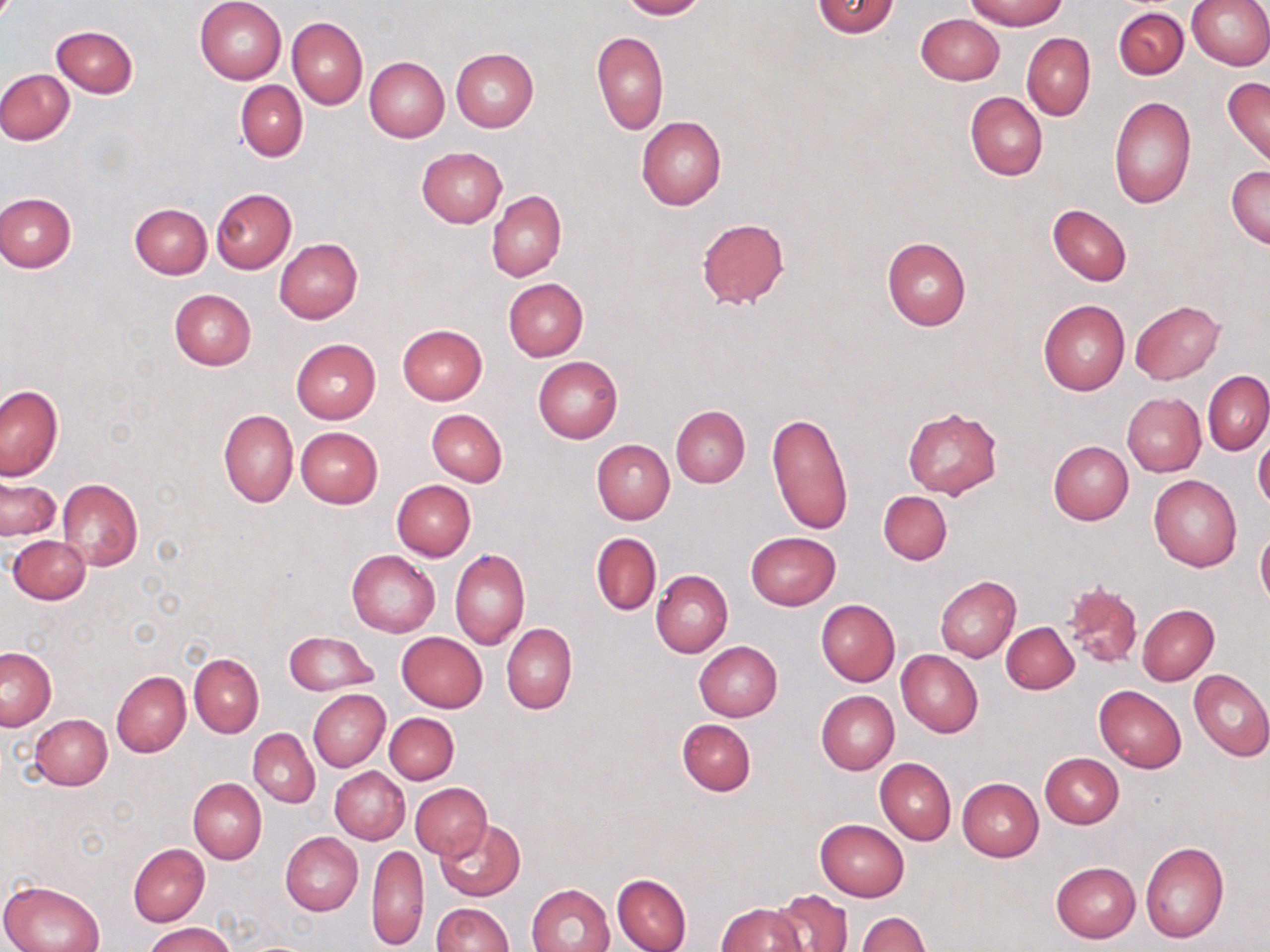
Approximate bounding boxes as named x1/y1/x2/y2 corners in pixels. Uninfected red blood cell locations: (x1=195, y1=0, x2=286, y2=84), (x1=620, y1=0, x2=704, y2=19), (x1=812, y1=0, x2=899, y2=38), (x1=964, y1=0, x2=1069, y2=30), (x1=1186, y1=0, x2=1270, y2=69), (x1=1114, y1=6, x2=1189, y2=79), (x1=916, y1=14, x2=1003, y2=85), (x1=287, y1=17, x2=367, y2=109), (x1=52, y1=25, x2=138, y2=98), (x1=591, y1=31, x2=669, y2=135), (x1=1021, y1=33, x2=1095, y2=120), (x1=452, y1=49, x2=539, y2=132), (x1=365, y1=57, x2=449, y2=141), (x1=0, y1=68, x2=74, y2=145), (x1=1222, y1=77, x2=1270, y2=168), (x1=235, y1=81, x2=307, y2=161), (x1=965, y1=91, x2=1047, y2=181), (x1=1109, y1=96, x2=1196, y2=209), (x1=636, y1=115, x2=728, y2=210), (x1=417, y1=146, x2=507, y2=228), (x1=1227, y1=165, x2=1270, y2=248), (x1=210, y1=188, x2=296, y2=274), (x1=487, y1=191, x2=567, y2=281), (x1=1, y1=192, x2=76, y2=272), (x1=130, y1=204, x2=211, y2=279), (x1=1048, y1=204, x2=1132, y2=286), (x1=696, y1=218, x2=789, y2=310), (x1=882, y1=237, x2=970, y2=330), (x1=275, y1=239, x2=362, y2=323), (x1=503, y1=278, x2=587, y2=362), (x1=169, y1=288, x2=256, y2=370), (x1=1038, y1=300, x2=1130, y2=394), (x1=1130, y1=300, x2=1225, y2=384), (x1=398, y1=324, x2=486, y2=405), (x1=291, y1=338, x2=381, y2=423), (x1=533, y1=356, x2=621, y2=443), (x1=1203, y1=371, x2=1269, y2=455), (x1=0, y1=385, x2=63, y2=480), (x1=1121, y1=392, x2=1205, y2=476), (x1=671, y1=406, x2=750, y2=487), (x1=902, y1=407, x2=1002, y2=499), (x1=218, y1=409, x2=298, y2=507), (x1=426, y1=409, x2=507, y2=487), (x1=766, y1=411, x2=853, y2=536), (x1=295, y1=426, x2=383, y2=508), (x1=1253, y1=428, x2=1270, y2=513), (x1=592, y1=439, x2=674, y2=524), (x1=1049, y1=441, x2=1133, y2=524), (x1=1148, y1=474, x2=1241, y2=572), (x1=1, y1=478, x2=62, y2=541), (x1=57, y1=478, x2=143, y2=572), (x1=391, y1=480, x2=475, y2=560), (x1=878, y1=490, x2=951, y2=565), (x1=1256, y1=527, x2=1270, y2=612), (x1=746, y1=532, x2=840, y2=609), (x1=591, y1=533, x2=661, y2=616), (x1=9, y1=535, x2=90, y2=604), (x1=449, y1=548, x2=529, y2=650), (x1=347, y1=551, x2=440, y2=637), (x1=651, y1=570, x2=733, y2=657), (x1=935, y1=575, x2=1020, y2=662), (x1=1061, y1=580, x2=1144, y2=670), (x1=816, y1=599, x2=900, y2=686), (x1=1138, y1=605, x2=1219, y2=685), (x1=1001, y1=622, x2=1079, y2=694), (x1=501, y1=623, x2=576, y2=715), (x1=283, y1=632, x2=377, y2=694), (x1=397, y1=632, x2=487, y2=712), (x1=693, y1=641, x2=782, y2=721), (x1=1, y1=648, x2=56, y2=730), (x1=896, y1=650, x2=984, y2=738), (x1=189, y1=653, x2=263, y2=737), (x1=112, y1=670, x2=191, y2=758), (x1=1188, y1=670, x2=1270, y2=763), (x1=1094, y1=685, x2=1186, y2=771), (x1=308, y1=689, x2=390, y2=769), (x1=816, y1=690, x2=899, y2=775), (x1=385, y1=712, x2=458, y2=785), (x1=28, y1=714, x2=112, y2=790), (x1=677, y1=718, x2=756, y2=795), (x1=248, y1=729, x2=319, y2=806), (x1=1041, y1=753, x2=1124, y2=828), (x1=874, y1=757, x2=956, y2=844), (x1=330, y1=766, x2=410, y2=844), (x1=188, y1=778, x2=266, y2=863), (x1=957, y1=778, x2=1044, y2=861), (x1=409, y1=782, x2=491, y2=859), (x1=814, y1=819, x2=908, y2=902), (x1=435, y1=820, x2=525, y2=901), (x1=281, y1=832, x2=363, y2=915), (x1=1139, y1=842, x2=1228, y2=944), (x1=128, y1=843, x2=209, y2=926), (x1=368, y1=843, x2=429, y2=950), (x1=1051, y1=861, x2=1141, y2=942), (x1=613, y1=874, x2=692, y2=952), (x1=0, y1=878, x2=105, y2=952), (x1=527, y1=883, x2=616, y2=952), (x1=772, y1=889, x2=852, y2=952), (x1=430, y1=903, x2=511, y2=952), (x1=715, y1=903, x2=808, y2=952), (x1=856, y1=912, x2=929, y2=951), (x1=144, y1=922, x2=236, y2=952). Slide-level diagnosis: no evidence of blood parasites. Optical microscopy. 1000x magnification. Image is 1270×952 pixels. Thin blood film. May-Grünwald-Giemsa-stained preparation. Single field of view.